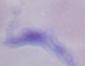
Captured at 1000x magnification. A trypanosome is seen. Photomicrograph.